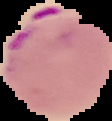
{
  "image_size": "112×121 pixels",
  "result": "malaria parasites identified",
  "image_type": "cell region segmented out of the field of view; surrounding area masked to black",
  "preparation": "thin blood film"
}